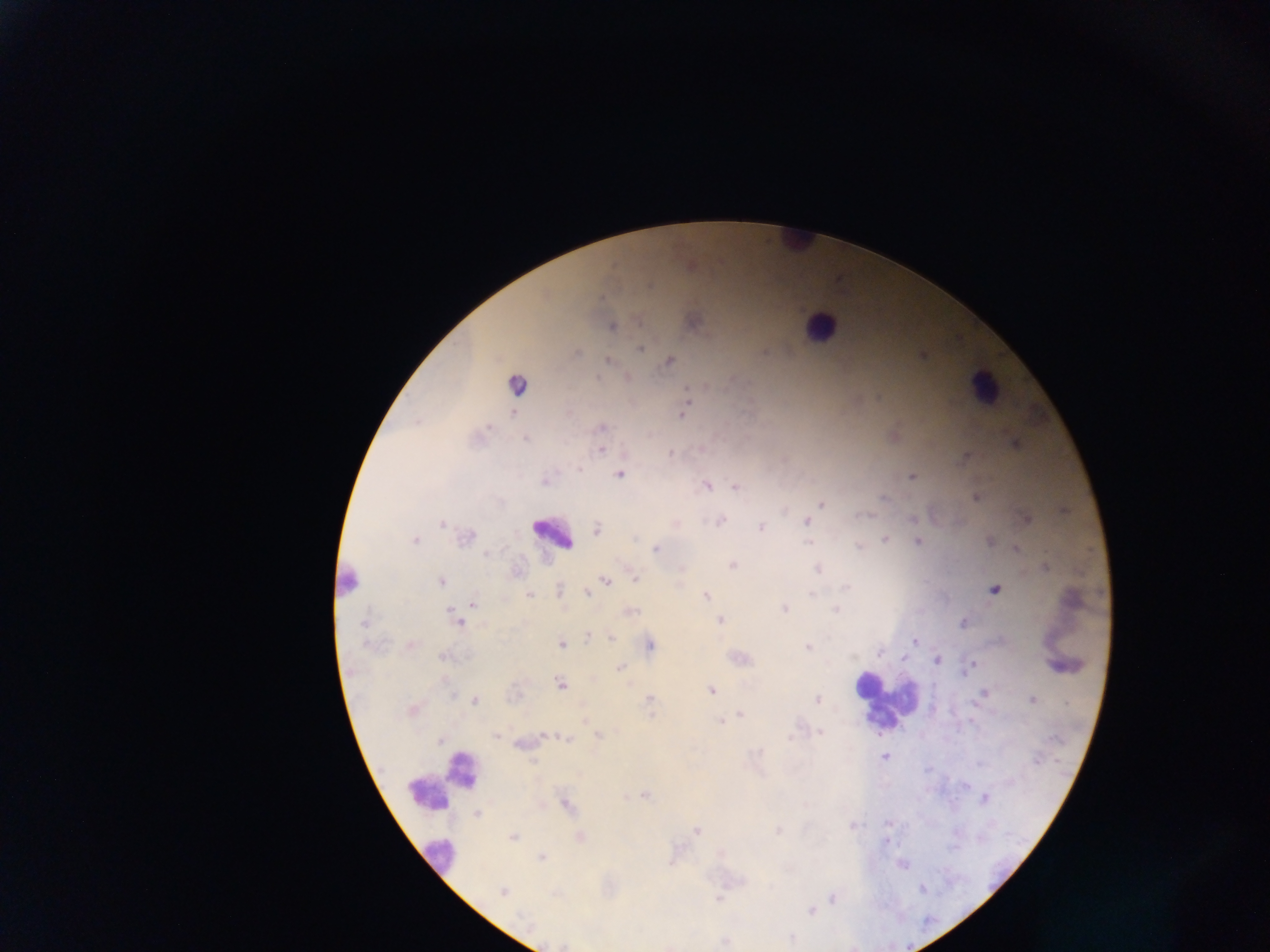

field_of_view: single
preparation: thick blood film
country: Ghana
image_size: 1270×952 pixels
capture: mobile-phone photograph through a microscope
leukocyte_locations: 'approximate centers as (x, y) in pixels: (798, 241), (820, 326), (983, 387), (551, 533), (345, 581), (867, 685), (885, 701), (442, 780), (438, 855)'
malaria_parasite_locations: 'approximate centers as (x, y) in pixels: (612, 326), (640, 348), (576, 353), (923, 355), (609, 361), (670, 361), (628, 377), (516, 385), (687, 389), (686, 397), (685, 407), (512, 412), (682, 414), (416, 421), (487, 427), (602, 427), (525, 439), (1014, 443), (601, 450), (671, 452), (967, 457), (578, 468), (619, 475), (911, 477), (544, 481), (706, 486), (735, 487), (975, 498), (884, 499), (822, 504), (912, 519), (720, 521), (806, 521), (442, 524), (761, 527), (596, 529), (466, 536), (885, 539), (414, 540), (989, 540), (808, 542), (918, 542), (859, 546), (1016, 548), (655, 549), (487, 555), (732, 564), (1045, 567), (817, 569), (636, 578), (605, 580), (440, 581), (846, 588), (559, 589), (995, 590), (588, 593), (811, 594), (529, 595), (705, 595), (474, 604), (783, 608), (836, 609), (631, 611), (456, 619), (719, 620), (363, 623), (964, 623), (588, 638), (612, 638), (914, 641), (412, 644), (561, 644), (650, 644), (807, 647), (879, 653), (444, 657), (904, 658), (937, 660), (972, 665), (620, 667), (560, 685), (711, 690), (984, 693), (649, 700), (817, 700), (1032, 700), (475, 701), (412, 710), (740, 715), (721, 720), (584, 721), (820, 732), (496, 736), (599, 736), (566, 740), (440, 741), (885, 757), (645, 796), (985, 799), (566, 806), (477, 813), (852, 825), (779, 830), (697, 831), (512, 838), (886, 841), (542, 858), (902, 865), (502, 891), (717, 898), (832, 898), (811, 911), (792, 937)'